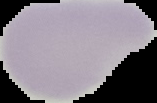
malaria status = uninfected
preparation = thin blood smear
image size = 157×103 pixels
image type = cell region segmented out of the field of view; surrounding area masked to black